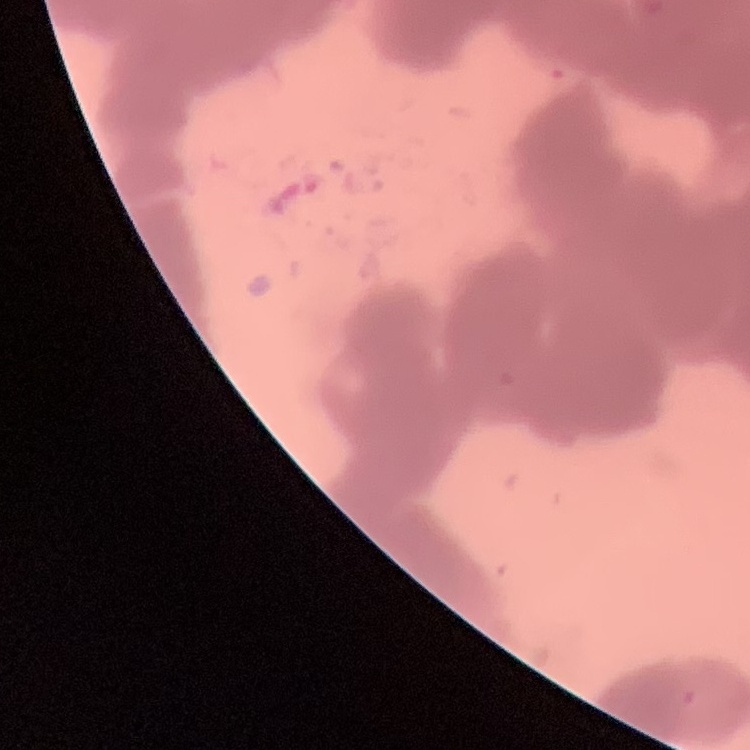

{
  "red_blood_cell_morphology": "rouleaux formation",
  "preparation": "thin blood smear",
  "stain": "Field's or Giemsa",
  "image_type": "one tile cut from a larger photomicrograph"
}